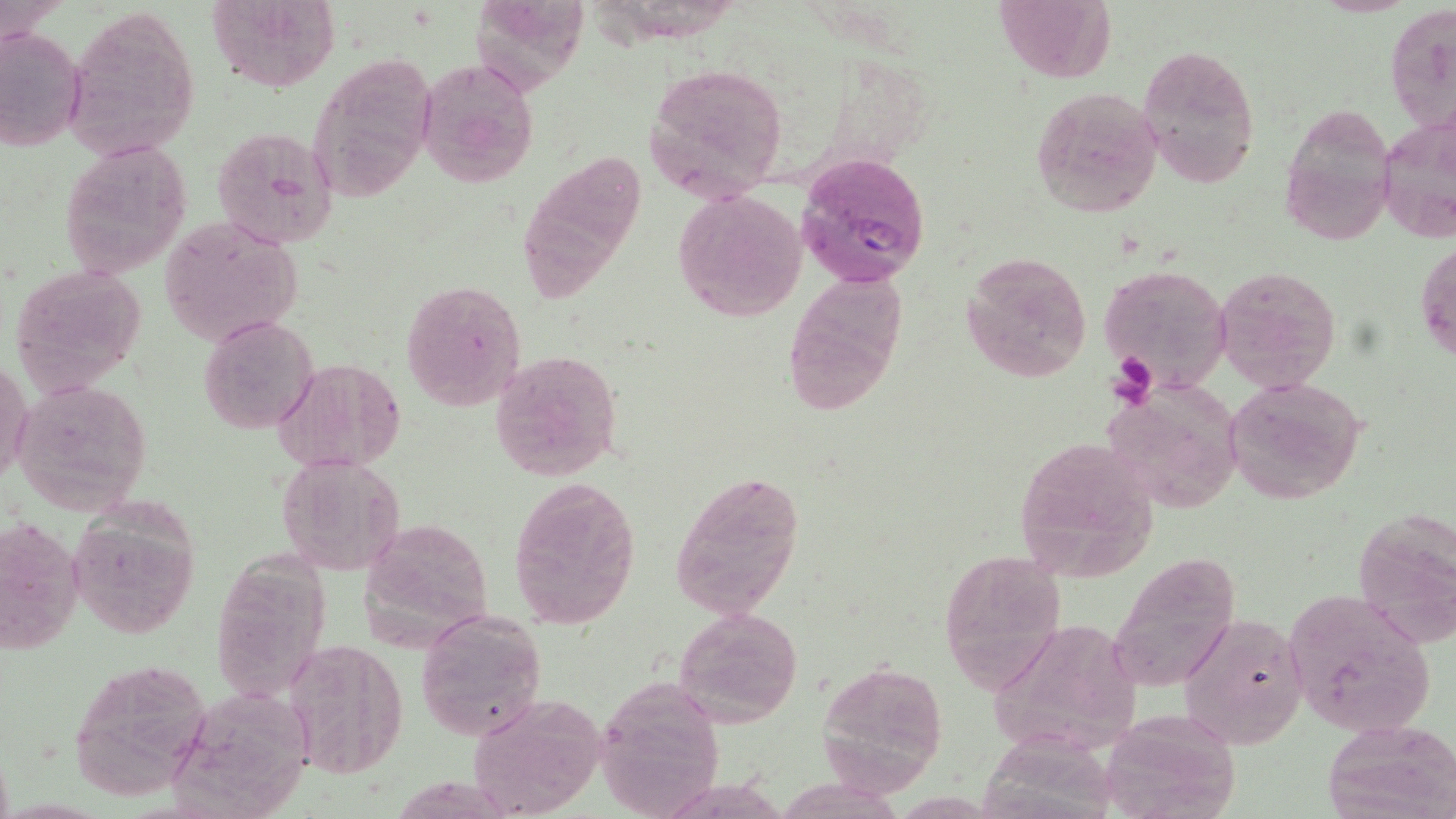
Summary:
  - Coordinate format: approximate bounding boxes as (x1, y1, x2, y2) in pixels
  - Platelet locations: (1106, 354, 1158, 406)
  - Plasmodium falciparum-infected red blood cell locations: (797, 152, 931, 288)
  - Uninfected red blood cell locations: (206, 0, 340, 91), (993, 0, 1115, 82), (1386, 2, 1456, 136), (63, 5, 199, 160), (0, 26, 84, 153), (1137, 46, 1260, 189), (307, 54, 438, 205), (416, 59, 539, 188), (644, 61, 787, 199), (1030, 86, 1163, 217), (1280, 102, 1395, 243), (1378, 112, 1456, 245), (210, 125, 339, 249), (58, 139, 189, 275), (519, 152, 650, 297), (672, 189, 807, 320), (160, 215, 304, 347), (1418, 236, 1455, 370), (962, 250, 1094, 383), (8, 263, 149, 398), (1098, 263, 1235, 394), (1214, 264, 1343, 395), (784, 272, 910, 416), (400, 281, 527, 413), (199, 315, 320, 433), (490, 350, 622, 482), (1, 356, 32, 489), (273, 359, 406, 475), (1226, 375, 1368, 504), (12, 379, 153, 517), (1108, 383, 1245, 514), (1010, 435, 1160, 581), (278, 455, 404, 574), (669, 466, 805, 620), (507, 475, 641, 629), (66, 502, 199, 639), (1353, 510, 1456, 649), (0, 514, 86, 660), (360, 514, 496, 644), (937, 551, 1063, 687), (1107, 553, 1244, 691), (1282, 589, 1436, 736), (674, 606, 803, 728), (1179, 609, 1309, 751), (414, 611, 547, 741), (989, 615, 1140, 759), (281, 640, 409, 780), (64, 658, 211, 801), (818, 661, 948, 792), (594, 675, 726, 818), (464, 695, 604, 817), (1327, 723, 1456, 816)
  - Slide-level diagnosis: Plasmodium falciparum
  - Magnification: 1000x
  - Stain: May-Grünwald-Giemsa
  - Preparation: thin blood smear
  - Image size: 1456×819 pixels
  - Field of view: single
  - Modality: light microscopy